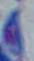 Toxoplasma gondii is seen. Photomicrograph. 1000x magnification.